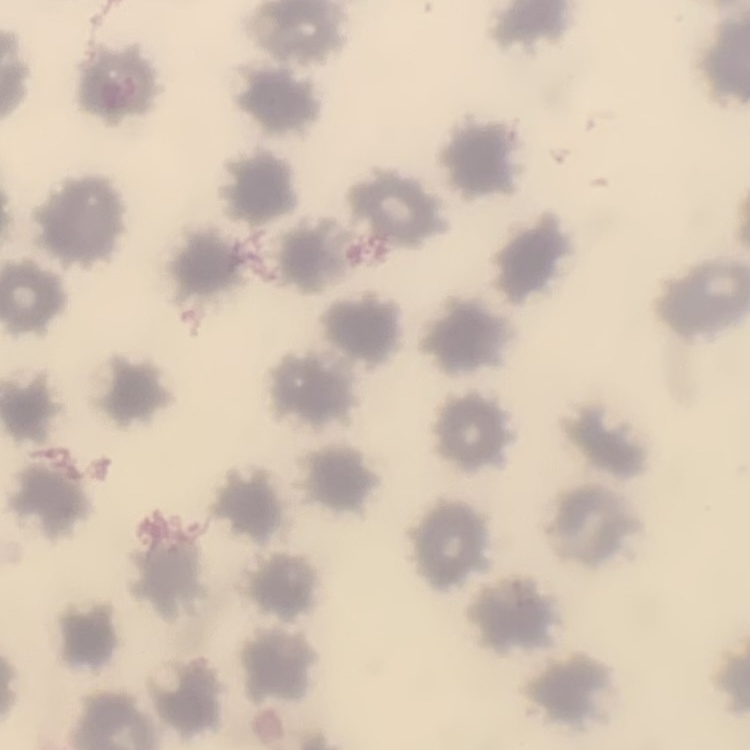 The red blood cells exhibit no rouleaux formation. One tile cut from a larger photomicrograph. Thin blood film. Stained with either Field's or Giemsa.